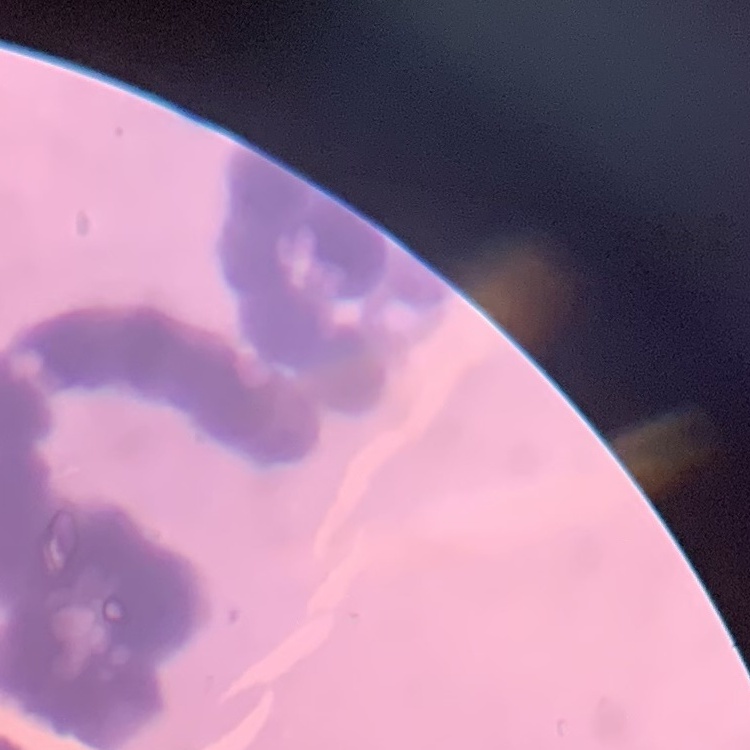
Summary:
  - Erythrocyte morphology: rouleaux formation
  - Stain: Field's or Giemsa
  - Image type: one tile cut from a larger photomicrograph
  - Preparation: thin blood smear